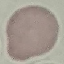
Summary:
  - Malaria status: uninfected
  - Stain: Giemsa
  - Image type: automatically extracted cell patch, resized to 64 × 64 pixels
  - Capture: smartphone camera at the microscope eyepiece
  - Preparation: thin smear